Report the malaria status of this cell.
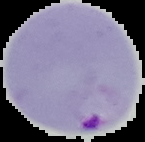
Parasitized.

From a thin blood film. Image is 145×142 pixels. Cell region segmented out of the field of view; the surrounding area is masked to black.